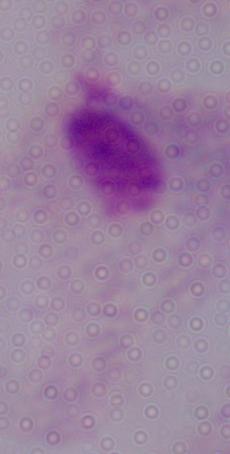

magnification = 1000x
modality = micrograph
identification = trichomonad